Outline each blood parasite and name the species.
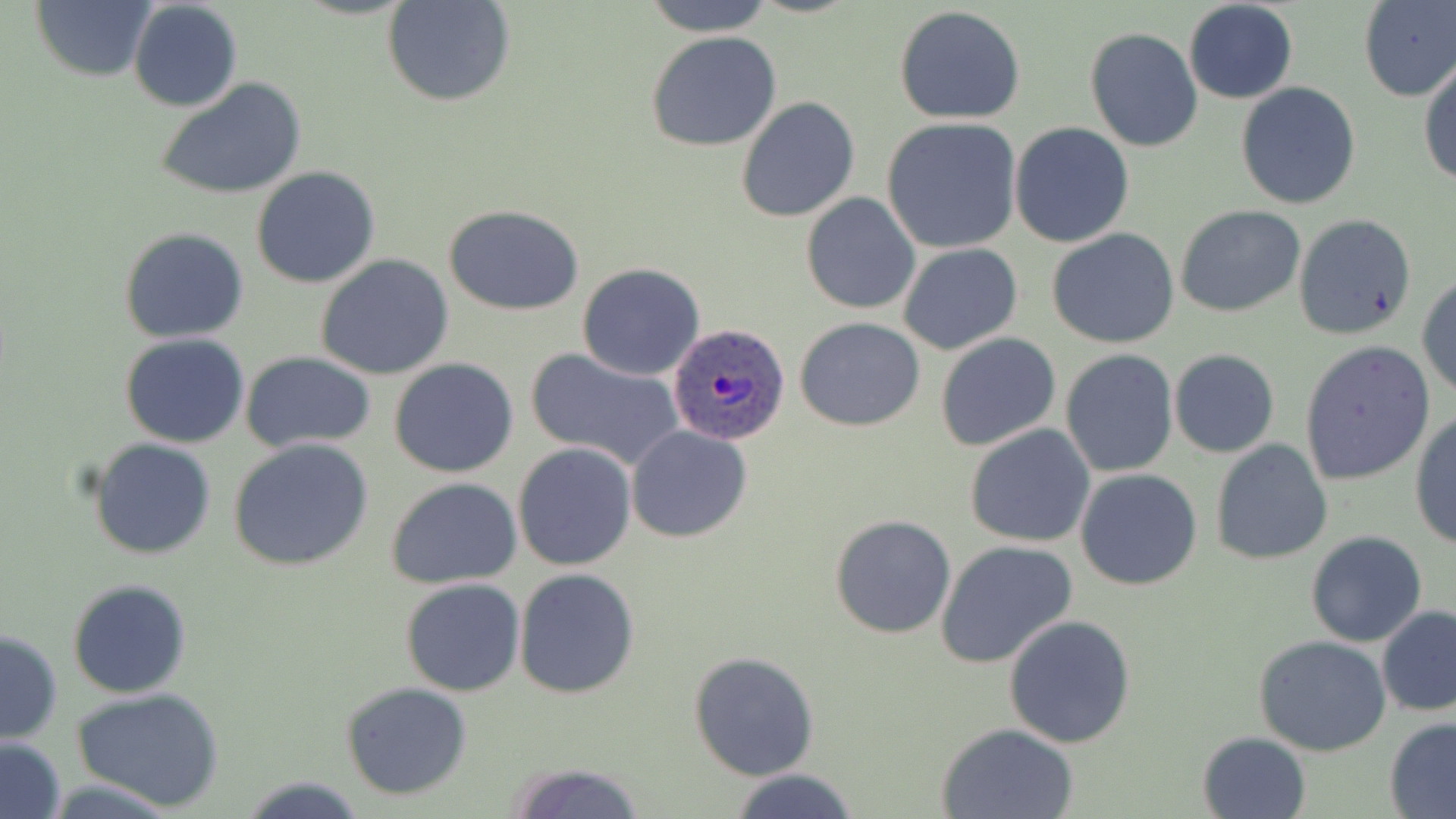

Approximate bounding boxes as [x1, y1, x2, y2] in pixels.
Plasmodium ovale-infected red blood cells: [667, 322, 791, 445].
No Plasmodium falciparum, Plasmodium malariae, Plasmodium vivax, Babesia divergens, or Trypanosoma brucei observed.

Summary:
  - Uninfected red blood cell locations: [641, 0, 778, 36], [27, 1, 156, 83], [129, 1, 242, 113], [384, 1, 515, 107], [1183, 1, 1298, 104], [1357, 1, 1455, 102], [895, 6, 1027, 125], [1084, 27, 1202, 153], [646, 31, 783, 151], [1418, 57, 1456, 188], [156, 78, 308, 200], [1234, 81, 1362, 210], [735, 96, 860, 224], [880, 117, 1024, 254], [1008, 122, 1135, 248], [250, 165, 380, 289], [800, 193, 921, 315], [443, 204, 586, 315], [1174, 204, 1307, 318], [1293, 213, 1417, 341], [119, 227, 251, 344], [1047, 228, 1181, 349], [897, 243, 1023, 355], [315, 254, 454, 381], [576, 263, 706, 381], [1417, 273, 1456, 402], [794, 316, 926, 432], [936, 332, 1061, 452], [119, 333, 251, 448], [1299, 341, 1436, 485], [525, 348, 685, 472], [1060, 349, 1179, 477], [1169, 349, 1280, 459], [241, 352, 376, 454], [389, 358, 520, 478], [1410, 409, 1456, 552], [965, 423, 1095, 547], [625, 425, 753, 544], [88, 438, 218, 558], [229, 439, 376, 573], [1209, 439, 1332, 566], [513, 442, 636, 571], [1074, 468, 1203, 591], [385, 477, 522, 590], [830, 514, 957, 639], [1304, 532, 1427, 647], [936, 541, 1077, 667], [512, 569, 639, 698], [67, 578, 194, 699], [400, 578, 526, 697], [1376, 607, 1456, 717], [1005, 614, 1137, 748], [1, 628, 63, 745], [1254, 634, 1393, 756], [688, 650, 819, 780], [339, 681, 474, 801], [71, 687, 226, 812], [1383, 717, 1456, 818], [936, 722, 1080, 818], [1197, 730, 1311, 818], [0, 736, 67, 819], [502, 761, 648, 818], [725, 769, 860, 819], [238, 777, 368, 816]
  - Slide-level diagnosis: Plasmodium ovale
  - Stain: May-Grünwald-Giemsa
  - Field of view: single
  - Modality: optical microscopy
  - Preparation: thin blood film
  - Image size: 1456×819 pixels
  - Magnification: 1000x